Assess this cell for malaria.
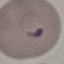
It is parasitized.

Acquired by smartphone through the microscope eyepiece. Cell patch, automatically extracted from a larger field of view and resized to 64 × 64 pixels. Giemsa stain. Thin smear of blood.